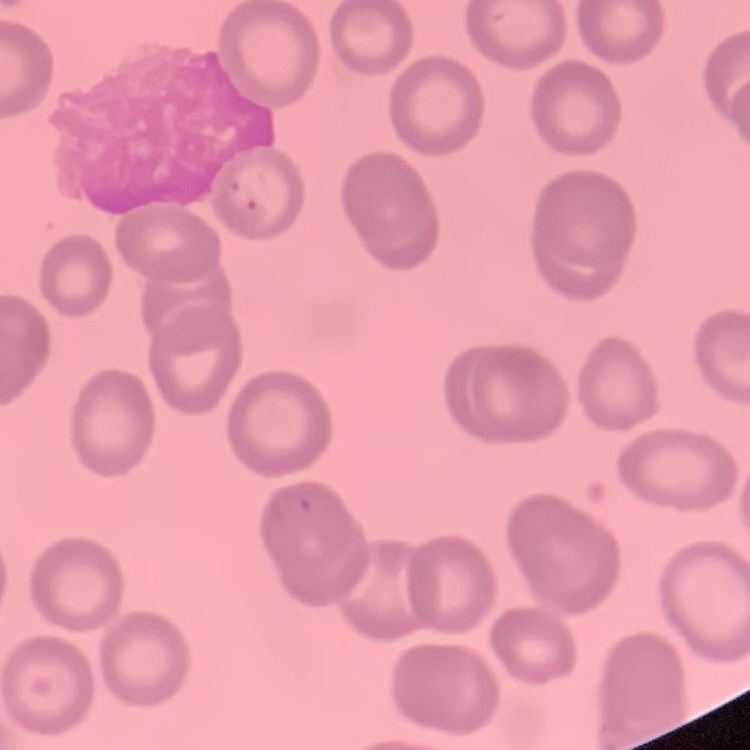
Summary:
  - Red blood cell morphology: no rouleaux formation
  - Stain: Field's or Giemsa
  - Image type: one tile cut from a larger photomicrograph
  - Preparation: thin peripheral smear